Comment on the morphology of the red blood cells.
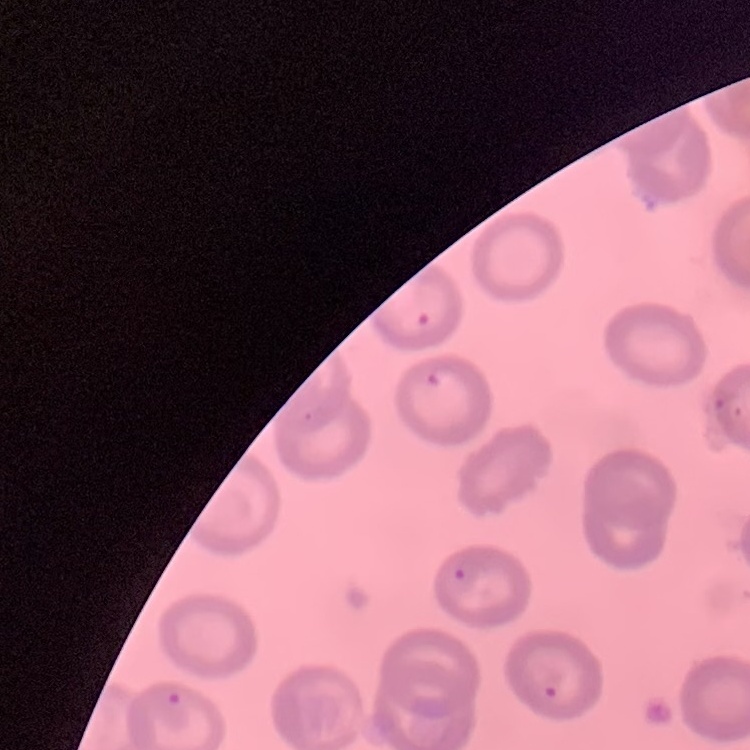

No rouleaux formation.

Summary:
  - Preparation: thin peripheral smear
  - Image type: square crop of a larger photomicrograph
  - Stain: Field's or Giemsa